Report the malaria status of this cell.
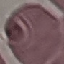

Uninfected.

stain = Giemsa
image type = automatically extracted cell patch, resized to 64 × 64 pixels
preparation = thin blood smear
capture = smartphone through the microscope eyepiece